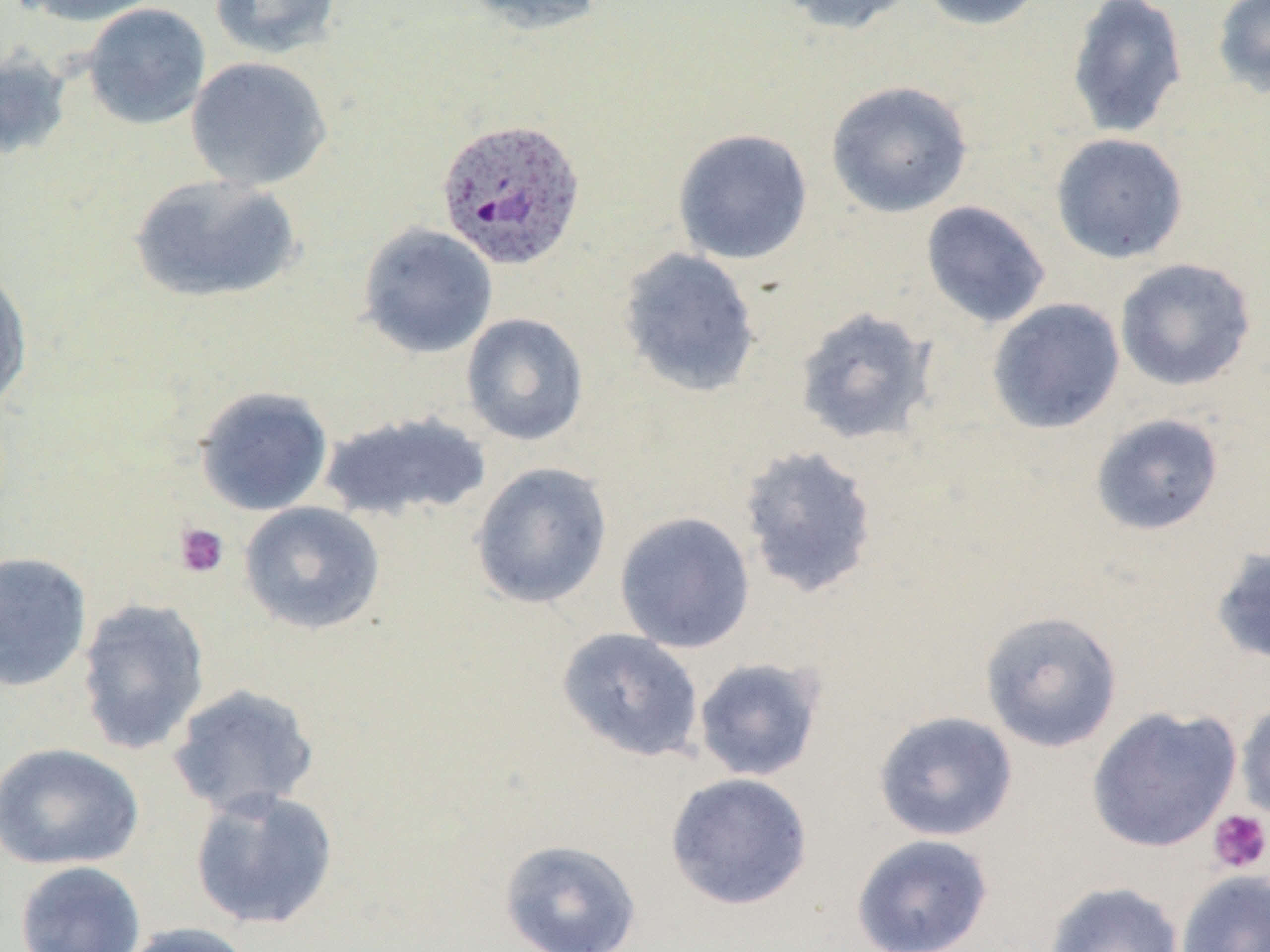
Approximate bounding boxes as (x1, y1, x2, y2) in pixels. Platelet locations: (173, 522, 229, 579), (1207, 808, 1270, 874). Plasmodium ovale-infected red blood cell locations: (435, 117, 587, 272). Uninfected red blood cell locations: (14, 0, 165, 26), (208, 0, 343, 59), (460, 0, 608, 36), (775, 0, 921, 35), (914, 0, 1050, 31), (1065, 0, 1188, 139), (1212, 0, 1270, 98), (81, 2, 211, 130), (0, 46, 74, 162), (185, 56, 333, 191), (825, 80, 973, 218), (672, 128, 813, 265), (1049, 133, 1189, 264), (128, 173, 302, 305), (920, 200, 1051, 329), (357, 223, 499, 359), (617, 247, 762, 398), (1114, 257, 1257, 392), (0, 265, 33, 413), (986, 297, 1126, 435), (793, 306, 938, 448), (461, 312, 589, 446), (194, 385, 333, 516), (320, 410, 492, 524), (1089, 412, 1225, 536), (737, 443, 880, 600), (469, 461, 612, 609), (238, 501, 386, 635), (614, 511, 756, 654), (1209, 544, 1270, 667), (0, 551, 93, 693), (76, 597, 211, 756), (979, 609, 1123, 753), (555, 627, 704, 763), (692, 656, 826, 782), (167, 683, 321, 819), (1235, 698, 1270, 826), (1086, 705, 1242, 853), (872, 710, 1018, 842), (1, 742, 145, 871), (664, 771, 814, 910), (189, 786, 339, 931), (851, 833, 994, 952), (498, 838, 643, 952), (14, 860, 146, 952), (1175, 869, 1270, 952), (1042, 881, 1184, 952), (116, 921, 257, 952). Slide-level diagnosis: Plasmodium ovale. Thin blood smear. Captured at 1000x magnification. May-Grünwald-Giemsa stain. Single field of view. Optical microscopy. Image is 1270×952 pixels.